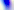

magnification: 400x
modality: photomicrograph
identification: Toxoplasma gondii